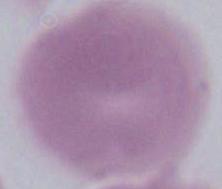

Summary:
  - Modality: photomicrograph
  - Magnification: 1000x
  - Identification: red blood cell